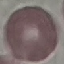
Summary:
  - Malaria status: uninfected
  - Image type: cell patch, automatically extracted from a larger field of view and resized to 64 × 64 pixels
  - Capture: smartphone camera at the microscope eyepiece
  - Stain: Giemsa
  - Preparation: thin smear